Locate platelets.
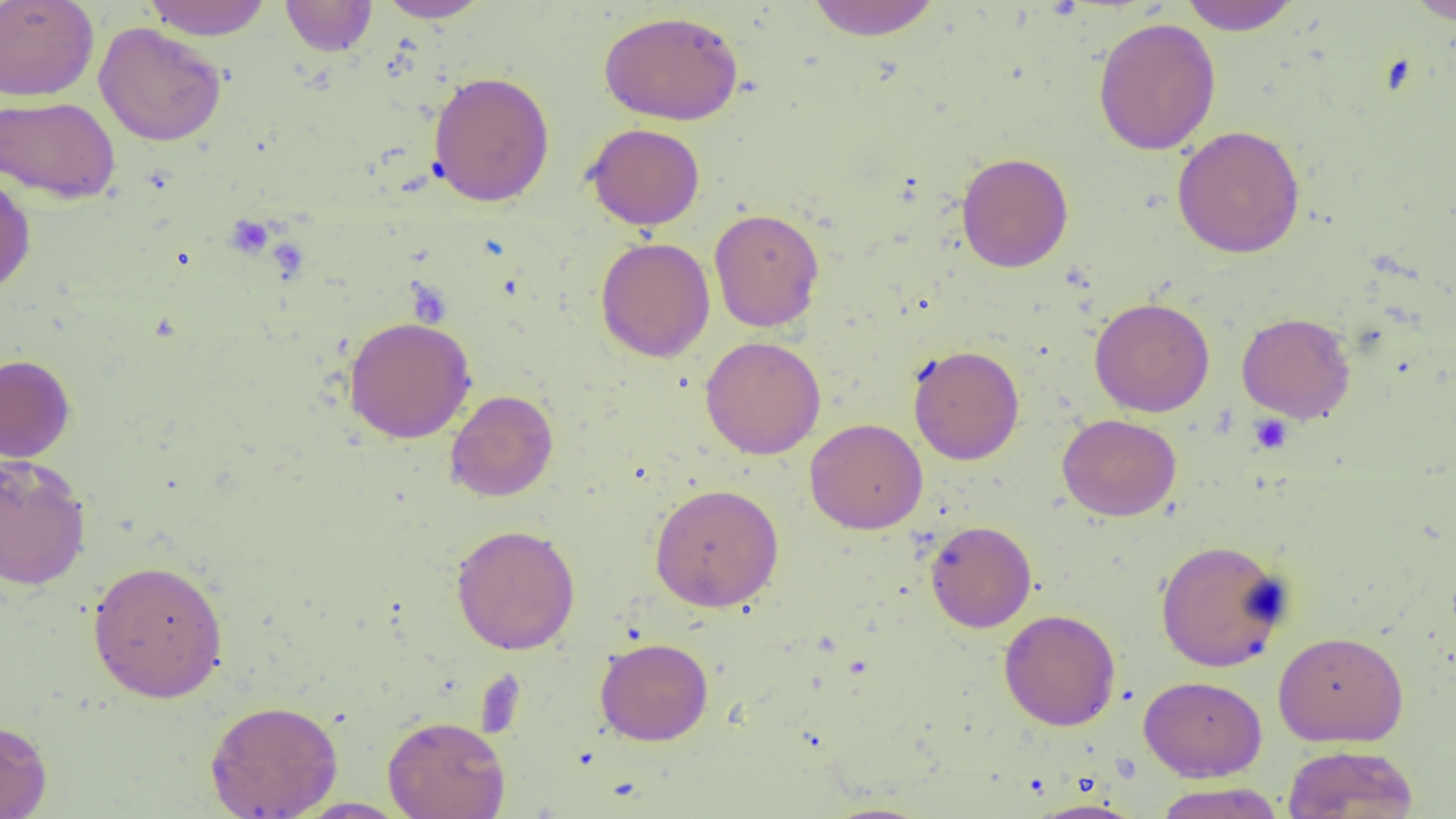

Approximate bounding boxes as (x1, y1, x2, y2) in pixels.
Platelets: (1249, 413, 1292, 453).

slide-level diagnosis = no evidence of blood parasites
image size = 1456×819 pixels
modality = optical microscopy
uninfected red blood cell locations = approximate bounding boxes as (x1, y1, x2, y2) in pixels: (0, 0, 99, 101), (142, 0, 273, 40), (280, 0, 377, 56), (377, 0, 493, 22), (805, 0, 943, 41), (1178, 0, 1302, 34), (1405, 0, 1455, 26), (598, 10, 744, 125), (1092, 17, 1221, 155), (94, 22, 228, 146), (428, 71, 555, 207), (0, 95, 120, 204), (585, 123, 705, 230), (1172, 125, 1306, 258), (955, 152, 1074, 273), (0, 170, 36, 296), (709, 208, 825, 332), (596, 237, 715, 362), (1089, 297, 1215, 416), (1236, 312, 1356, 424), (343, 316, 476, 443), (701, 335, 826, 460), (908, 344, 1024, 465), (0, 353, 77, 462), (445, 389, 558, 502), (1057, 413, 1182, 521), (805, 417, 928, 534), (0, 453, 91, 590), (649, 483, 785, 612), (925, 520, 1037, 633), (451, 524, 580, 655), (1154, 538, 1291, 672), (86, 558, 229, 703), (999, 609, 1120, 731), (1272, 630, 1409, 747), (595, 637, 714, 746), (1139, 675, 1267, 782), (205, 699, 343, 818), (382, 715, 511, 819), (0, 717, 52, 819), (1282, 744, 1419, 818), (1153, 782, 1286, 819), (291, 798, 412, 818), (1025, 799, 1146, 818), (815, 802, 938, 819)
magnification = 1000x
preparation = thin blood film
field of view = single